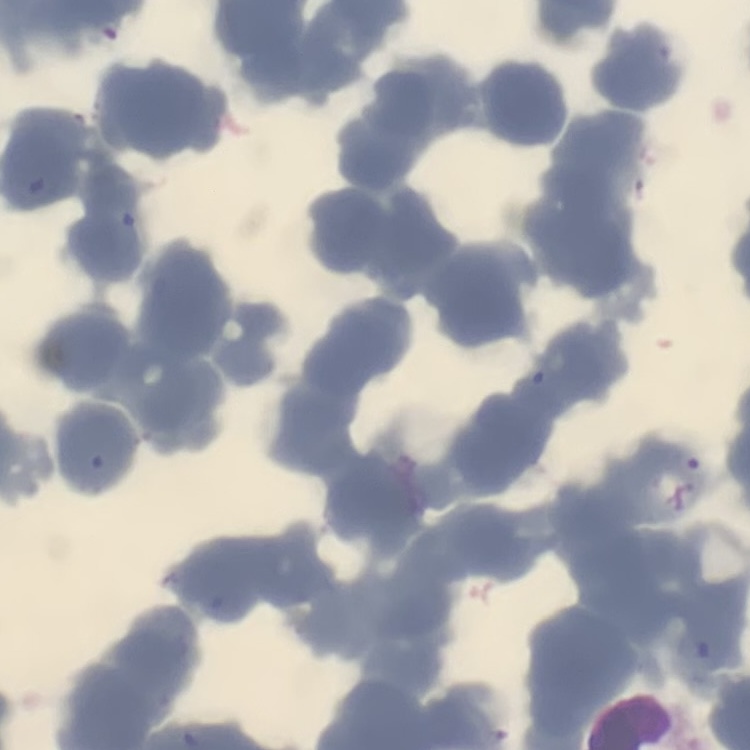

red_blood_cell_morphology: rouleaux formation
stain: Field's or Giemsa
image_type: one tile cut from a larger photomicrograph
preparation: thin blood film